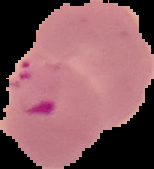
Summary:
  - Image size: 154×169 pixels
  - Image type: cell region segmented out of the field of view; surrounding area masked to black
  - Preparation: thin blood smear
  - Result: malaria parasites detected